Comment on the morphology of the erythrocytes.
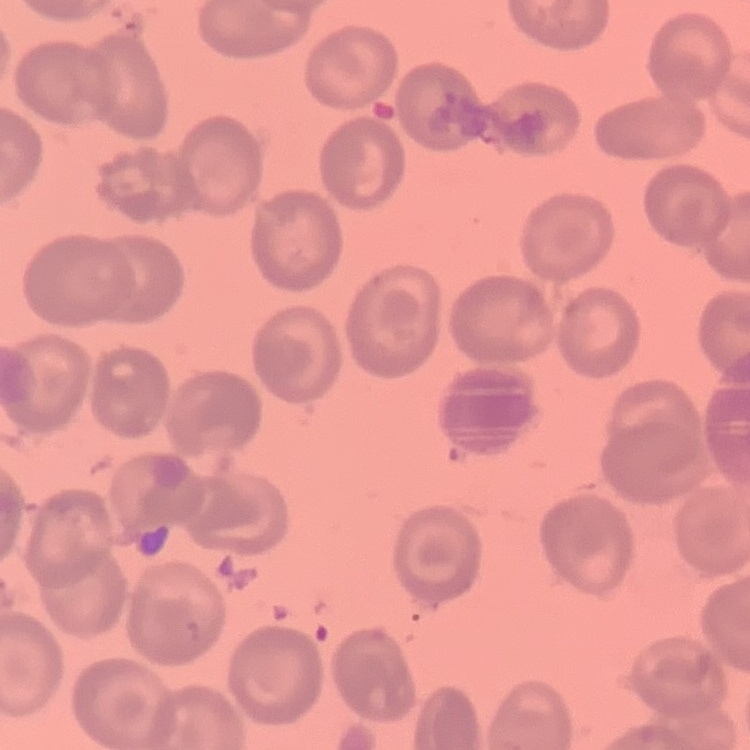
They show no rouleaux formation.

Summary:
  - Image type: square crop of a larger photomicrograph
  - Stain: Field's or Giemsa
  - Preparation: thin peripheral smear